Locate every leukocyte (white blood cell).
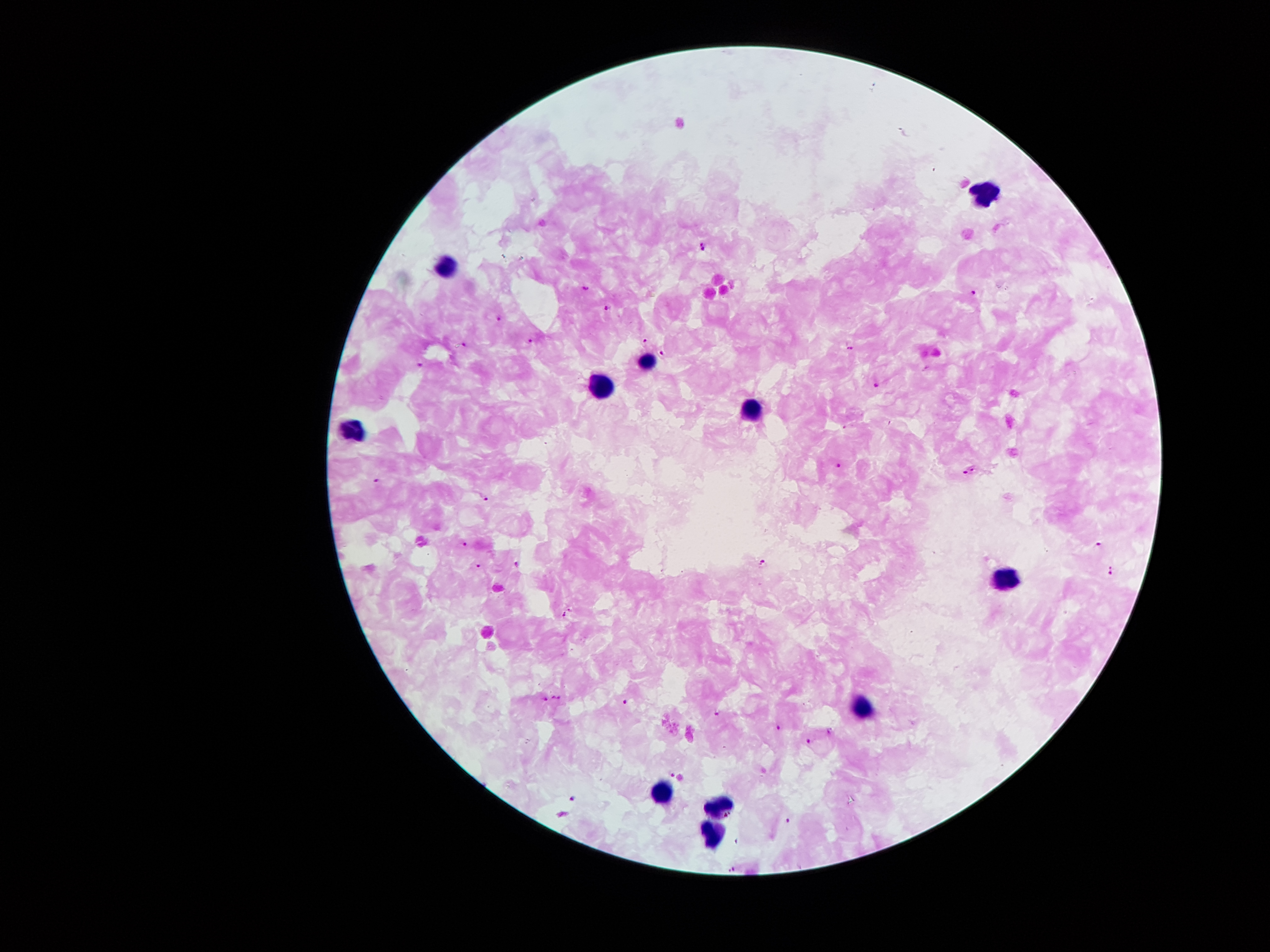

Approximate centers as {x, y} in pixels.
Leukocytes: {984, 191}, {446, 268}, {647, 360}, {602, 388}, {750, 405}, {352, 428}, {1006, 575}, {864, 707}, {663, 790}, {719, 799}, {712, 835}.

Plasmodium parasite locations: {703, 245}, {585, 288}, {975, 293}, {607, 307}, {499, 317}, {647, 338}, {466, 341}, {531, 341}, {852, 348}, {663, 354}, {421, 365}, {876, 384}, {839, 464}, {973, 469}, {965, 473}, {377, 481}, {487, 497}, {466, 541}, {1099, 544}, {763, 562}, {517, 564}, {478, 566}, {1112, 570}, {567, 613}, {552, 697}, {560, 698}, {546, 699}, {626, 702}, {717, 712}, {779, 728}, {830, 732}, {809, 741}, {673, 775}, {573, 797}, {786, 821}, {732, 867}. Thick blood smear. Patient malaria status: infected with Plasmodium falciparum. Giemsa stain. One field from this slide. Photographed through the microscope eyepiece with a smartphone camera. Image is 1270×952 pixels. 100x magnification.